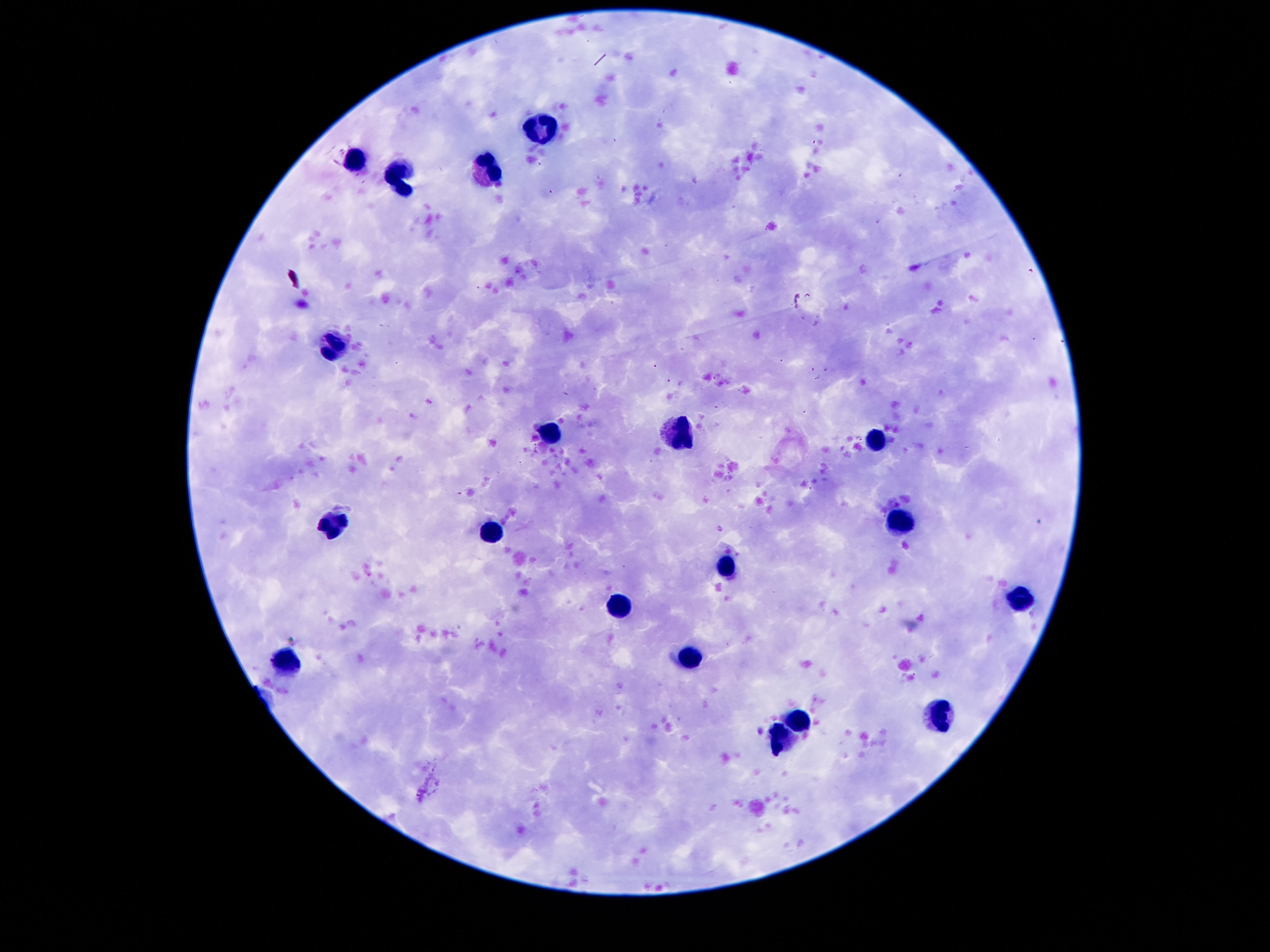

Approximate centers as [x, y] in pixels. Leukocyte locations: [539, 127], [356, 164], [488, 169], [400, 175], [336, 344], [550, 434], [683, 436], [877, 437], [334, 523], [898, 525], [491, 532], [727, 567], [1019, 600], [619, 609], [688, 658], [285, 660], [939, 711], [793, 722], [778, 739]. 100x magnification. Patient malaria status: uninfected. Smartphone photograph taken through the microscope eyepiece. Giemsa stain. One field from this slide. Thick blood smear. Image is 1270×952 pixels.